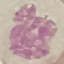
Summary:
  - Malaria status: uninfected
  - Capture: smartphone through the microscope eyepiece
  - Image type: automatically extracted cell patch, resized to 64 × 64 pixels
  - Stain: Giemsa
  - Preparation: thin blood film